Classify this cell by malaria status.
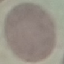

Uninfected.

{
  "capture": "smartphone camera at the microscope eyepiece",
  "preparation": "thin smear",
  "stain": "Giemsa",
  "image_type": "cell patch, automatically extracted from a larger field of view and resized to 64 × 64 pixels"
}